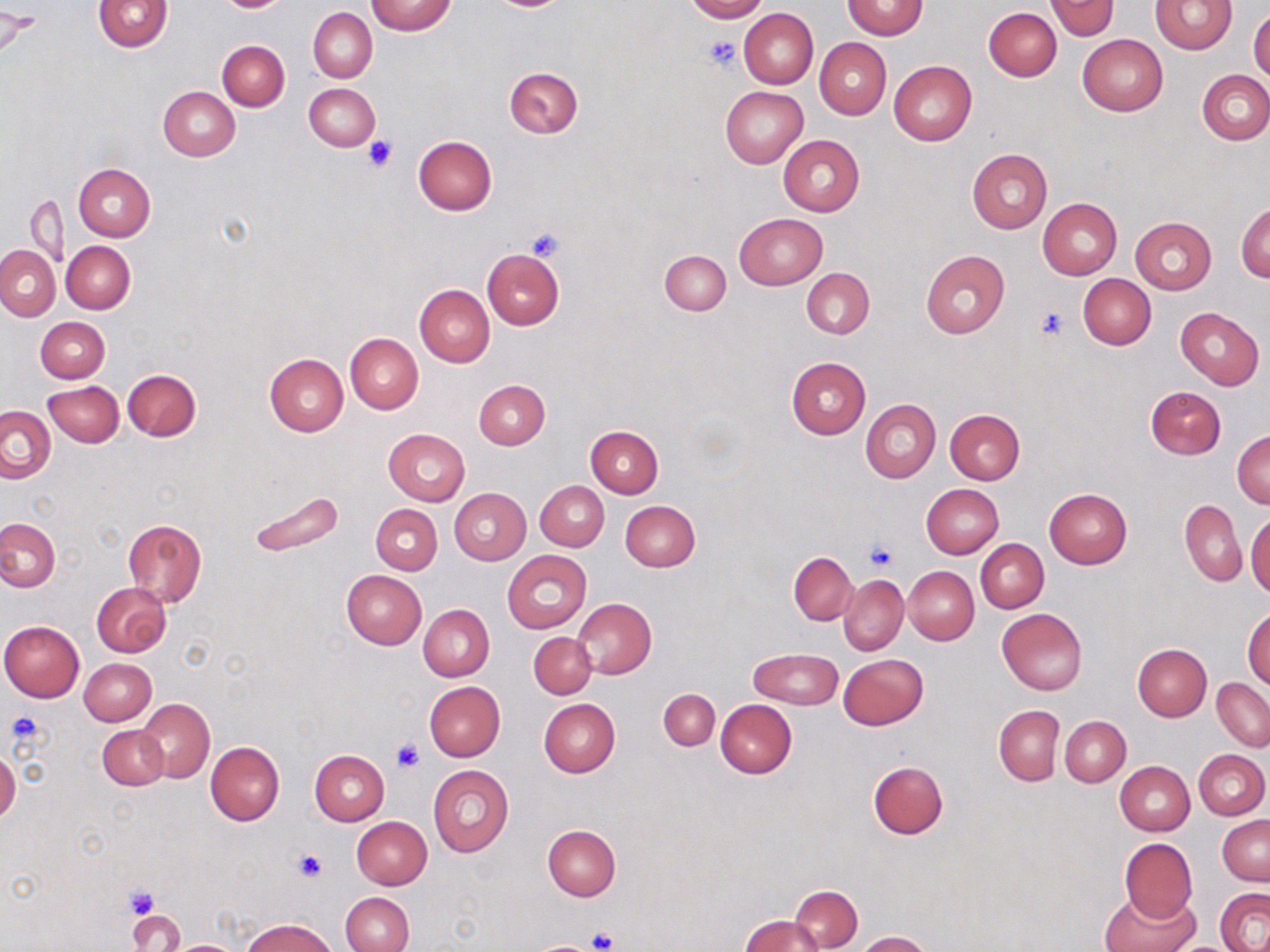

Approximate bounding boxes as (x1,y1)-(x2,y2) corner pairs in pixels. Platelet locations: (703,36)-(742,72), (362,136)-(399,172), (525,229)-(563,261), (1034,306)-(1071,341), (864,539)-(898,571), (5,710)-(43,750), (393,740)-(424,772), (294,850)-(327,883), (123,885)-(159,919), (587,927)-(620,952), (535,939)-(600,952). Uninfected red blood cell locations: (93,0)-(173,52), (217,0)-(288,12), (367,0)-(455,35), (684,0)-(768,22), (1046,0)-(1119,40), (842,1)-(927,39), (1150,1)-(1239,54), (984,6)-(1062,81), (309,7)-(377,82), (739,8)-(818,88), (1248,8)-(1270,83), (1,10)-(37,57), (1078,34)-(1167,115), (815,38)-(891,119), (217,40)-(289,110), (889,60)-(977,146), (504,66)-(583,138), (1198,70)-(1270,144), (304,83)-(380,151), (158,86)-(240,161), (720,86)-(808,167), (414,136)-(496,215), (779,136)-(865,217), (966,149)-(1053,233), (74,163)-(156,241), (70,166)-(143,314), (24,196)-(69,265), (1038,199)-(1122,278), (1236,203)-(1270,282), (735,213)-(826,289), (1131,217)-(1216,293), (61,241)-(136,313), (0,245)-(59,319), (483,248)-(564,329), (659,249)-(730,314), (921,250)-(1009,338), (802,269)-(874,338), (1077,274)-(1156,350), (415,284)-(495,366), (1175,307)-(1264,389), (36,316)-(110,383), (345,333)-(423,413), (264,352)-(348,436), (786,357)-(870,439), (123,369)-(201,441), (474,380)-(550,449), (43,381)-(123,448), (1146,386)-(1226,460), (860,399)-(940,483), (0,406)-(56,482), (945,409)-(1024,485), (585,427)-(663,498), (383,429)-(469,506), (1233,430)-(1269,509), (536,481)-(608,551), (921,484)-(1003,558), (450,488)-(530,565), (1043,488)-(1133,568), (247,490)-(344,558), (1180,499)-(1246,587), (620,500)-(700,571), (371,503)-(442,574), (1246,507)-(1269,596), (0,518)-(59,592), (122,518)-(206,607), (976,539)-(1048,612), (502,551)-(590,632), (789,553)-(856,625), (903,566)-(979,645), (342,570)-(426,649), (839,575)-(908,654), (92,583)-(171,657), (573,598)-(656,678), (418,604)-(494,681), (1243,606)-(1270,689), (997,608)-(1088,695), (528,619)-(646,691), (0,621)-(84,701), (529,632)-(596,699), (1132,643)-(1210,721), (750,648)-(842,709), (838,654)-(929,730), (79,658)-(156,726), (1211,678)-(1269,750), (424,681)-(505,761), (658,689)-(719,750), (538,698)-(620,777), (137,699)-(214,782), (716,699)-(797,779), (993,704)-(1063,785), (1060,716)-(1130,786), (98,725)-(168,789), (205,741)-(284,825), (1194,749)-(1269,819), (309,750)-(389,825), (0,752)-(19,822), (868,760)-(948,839), (1115,761)-(1194,835), (429,766)-(514,857), (1218,815)-(1270,886), (351,816)-(431,889), (543,824)-(621,900), (1119,838)-(1196,922), (789,884)-(863,950), (1215,889)-(1270,952), (1098,890)-(1199,952), (341,892)-(414,952), (127,909)-(183,951), (740,915)-(827,952), (243,918)-(335,952), (856,931)-(931,952), (169,940)-(241,951). Slide-level diagnosis: negative for blood parasites. Image is 1270×952 pixels. 1000x magnification. Thin blood smear. May-Grünwald-Giemsa stain. One field of a larger specimen. Light microscopy.